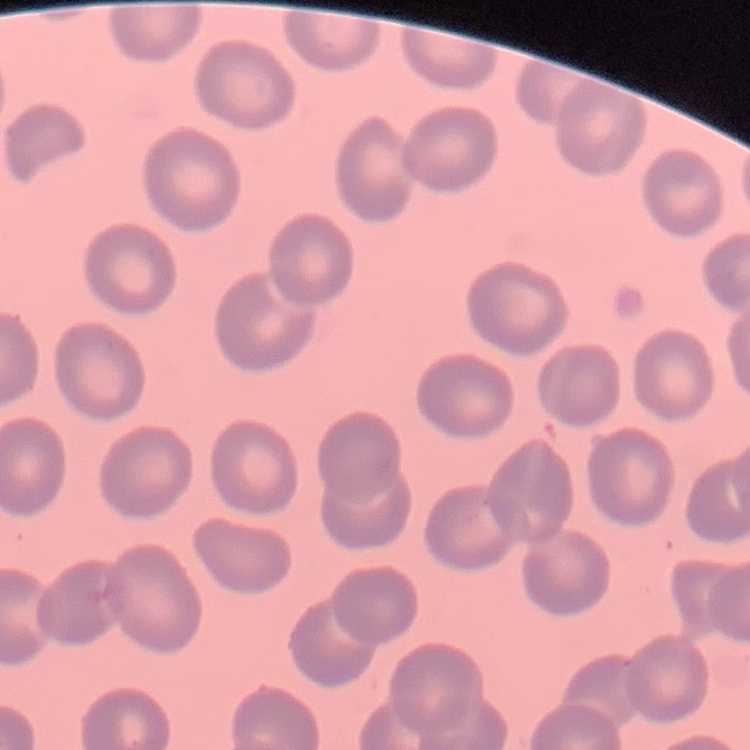
red_blood_cell_morphology: no rouleaux formation
stain: Field's or Giemsa
image_type: square crop of a larger photomicrograph
preparation: thin peripheral smear